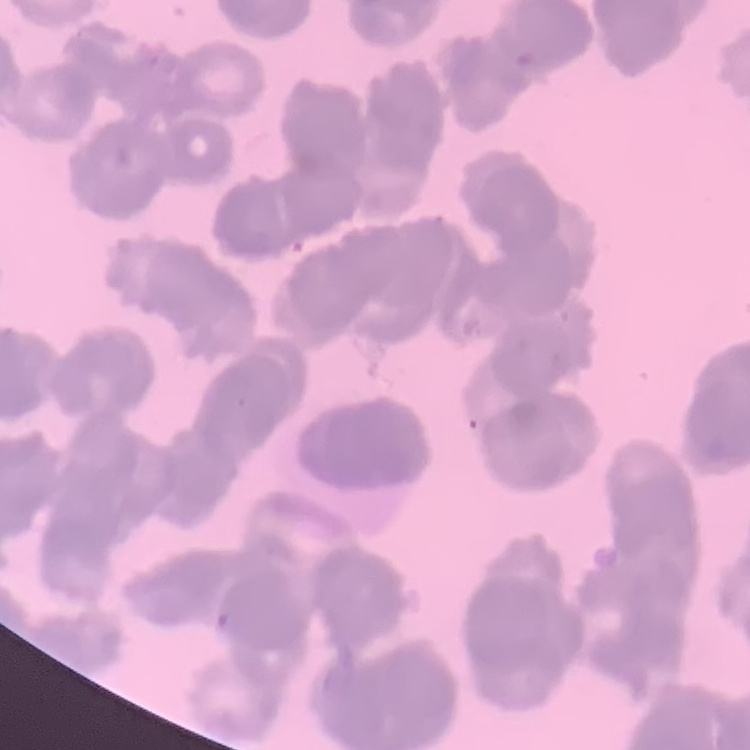
erythrocyte morphology = rouleaux formation
stain = Field's or Giemsa
image type = square crop of a larger photomicrograph
preparation = thin blood film